Find the red blood cells that are infected with Plasmodium falciparum, and any of indeterminate infection status.
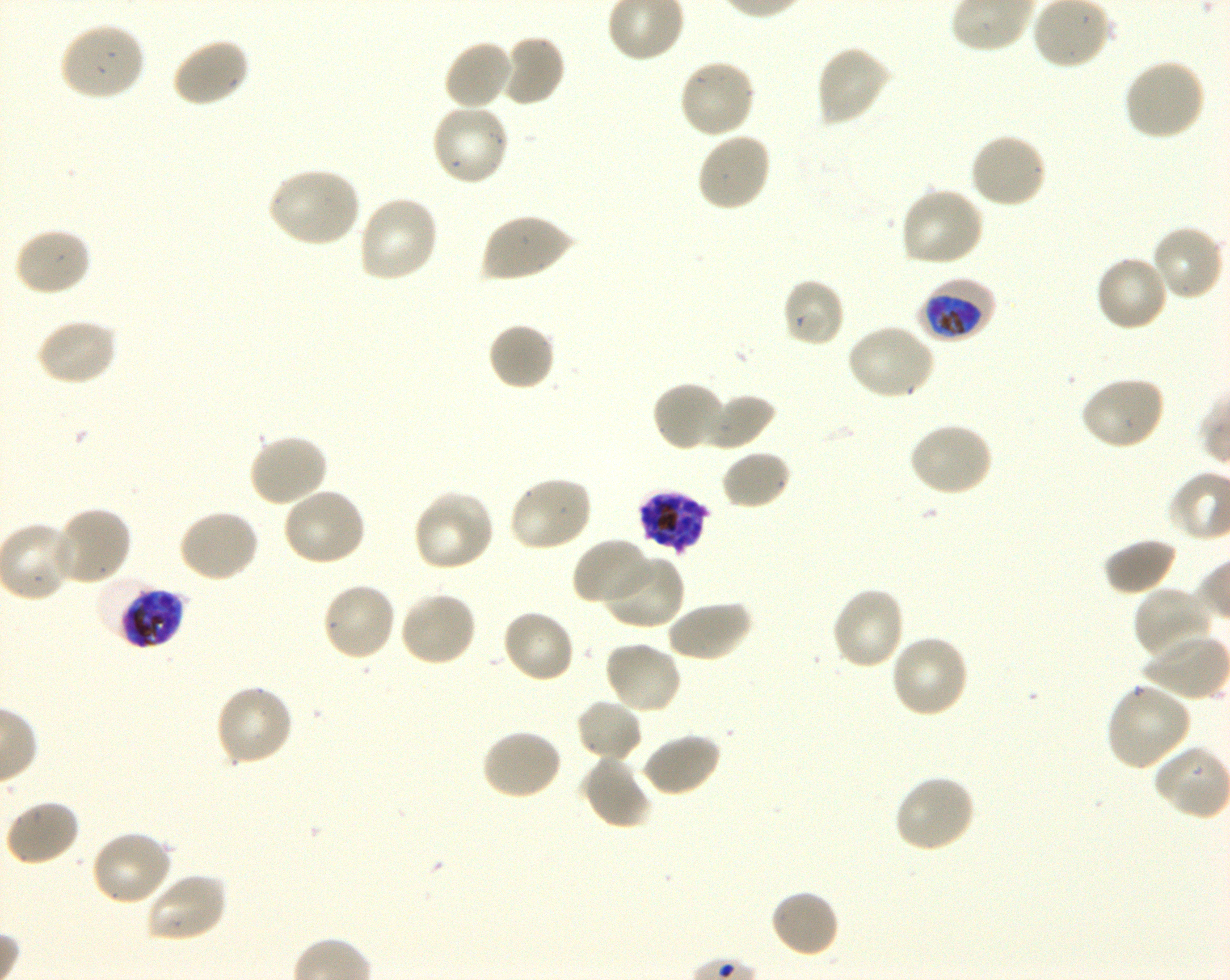
Approximate bounding boxes as (x1, y1, x2, y2) in pixels. Not every red blood cell is marked. A life-cycle stage — or a range of stages, where the recorded stages span more than one — follows each staged infected red blood cell.
Infected red blood cells: (918, 277, 996, 342) early trophozoite to early schizont; (636, 490, 710, 554); (96, 576, 175, 647) late trophozoite to late schizont.
No red blood cells of indeterminate infection status observed.

locations of uninfected red blood cells = (57, 22, 146, 102), (499, 33, 566, 107), (169, 35, 251, 108), (442, 38, 514, 111), (815, 44, 891, 127), (677, 58, 757, 140), (1122, 58, 1206, 142), (430, 102, 511, 187), (695, 130, 772, 213), (969, 132, 1048, 209), (267, 166, 362, 248), (899, 187, 986, 269), (357, 194, 440, 284), (480, 212, 575, 283), (1150, 224, 1226, 302), (13, 225, 92, 297), (1094, 255, 1170, 334), (781, 276, 846, 348), (34, 317, 118, 387), (487, 322, 556, 392), (845, 323, 935, 401), (1078, 375, 1166, 451), (651, 380, 727, 452), (699, 393, 775, 451), (908, 421, 994, 498), (247, 432, 330, 508), (720, 449, 792, 511), (507, 476, 594, 553), (281, 486, 368, 567), (412, 490, 496, 573), (51, 505, 133, 586), (177, 507, 261, 583), (570, 537, 656, 608), (1102, 537, 1178, 596), (603, 553, 685, 630), (321, 582, 397, 663), (830, 586, 906, 671), (1132, 586, 1215, 662), (397, 591, 477, 668), (665, 600, 752, 663), (501, 608, 576, 685), (889, 633, 970, 719), (1139, 634, 1228, 701), (603, 641, 683, 716), (1105, 682, 1192, 772), (214, 684, 295, 768), (574, 698, 644, 763), (480, 728, 564, 802), (639, 731, 722, 798), (579, 755, 653, 831), (893, 773, 977, 854), (4, 798, 81, 867), (89, 828, 174, 907), (143, 870, 228, 943), (769, 888, 841, 960)
preparation = thin blood film
field of view = one from this slide
image size = 1230×980 pixels
stain = Giemsa
donor blood group = O+
objective = 100x, oil immersion, numerical aperture 1.30
culture = in-vitro Plasmodium falciparum strain 3D7, shaking